Point out each malaria parasite and each leukocyte.
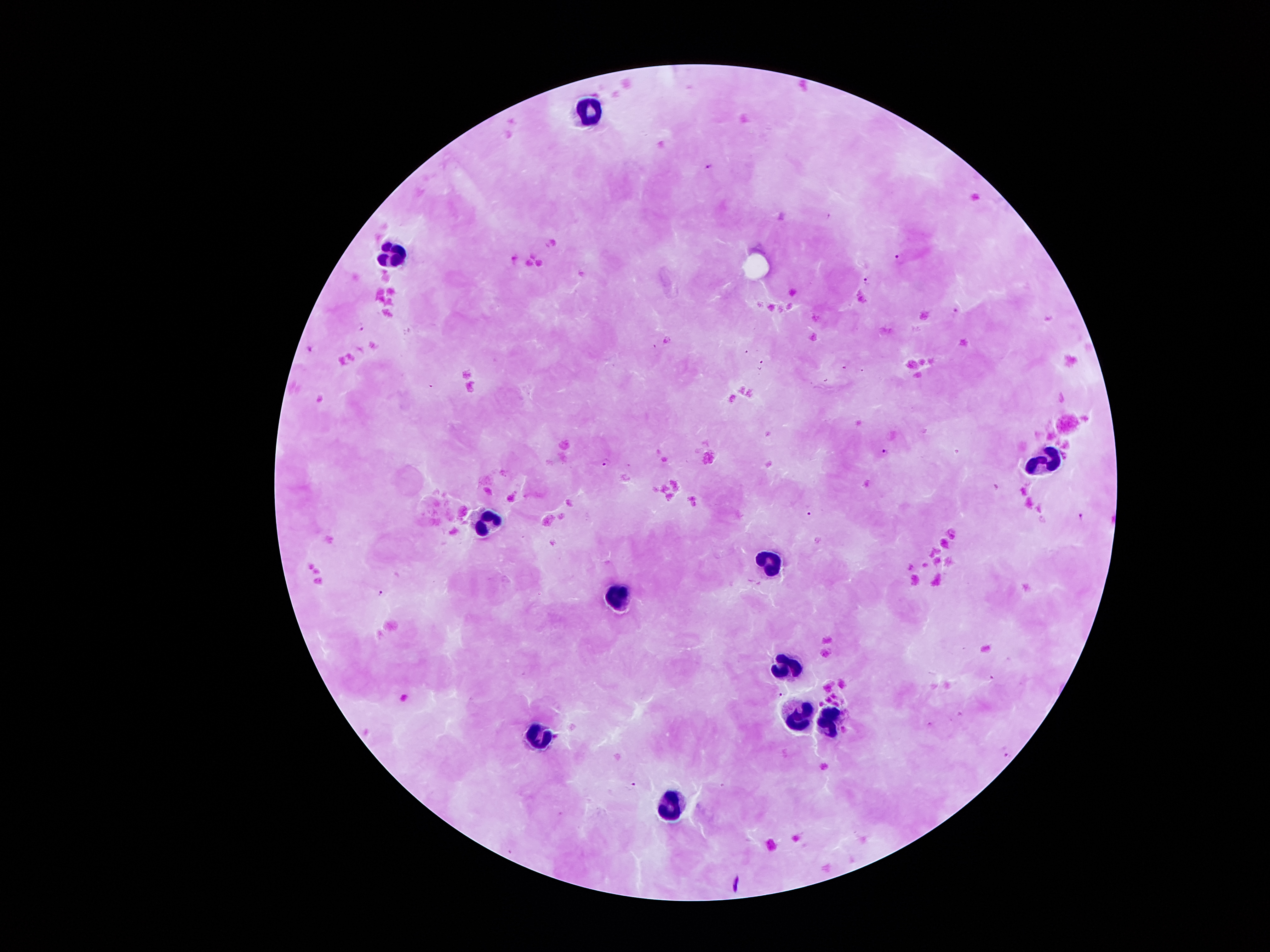
Approximate centers as [x, y] in pixels.
Malaria parasites: [711, 167], [900, 258], [866, 281], [957, 310], [360, 327], [884, 452], [608, 463], [811, 514], [1081, 517], [380, 593], [779, 695], [1006, 754], [633, 786].
Leukocytes: [591, 111], [394, 254], [1045, 464], [487, 523], [762, 569], [619, 596], [784, 666], [799, 712], [833, 720], [539, 736], [673, 805].

image size = 1270×952 pixels
field of view = single
preparation = thick blood smear
patient malaria status = infected with Plasmodium falciparum
stain = Giemsa
magnification = 100x
capture = smartphone through the microscope eyepiece